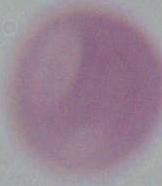
identification = erythrocyte
magnification = 1000x
modality = photomicrograph